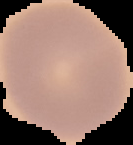

result = no malaria parasites detected
image size = 133×145 pixels
preparation = thin blood film
image type = segmented cell region on a black background